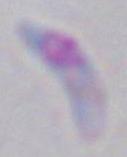
Captured at 1000x magnification. Photomicrograph. Toxoplasma gondii is seen.